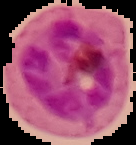

Summary:
  - Image size: 136×145 pixels
  - Preparation: thin blood smear
  - Malaria status: parasitized
  - Image type: cell region segmented out of the field of view; surrounding area masked to black